Assess this cell for malaria.
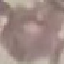
Uninfected.

Summary:
  - Preparation: thin blood film
  - Capture: smartphone through the microscope eyepiece
  - Stain: Giemsa
  - Image type: cell patch, automatically extracted from a larger field of view and resized to 64 × 64 pixels